State which parasite is depicted.
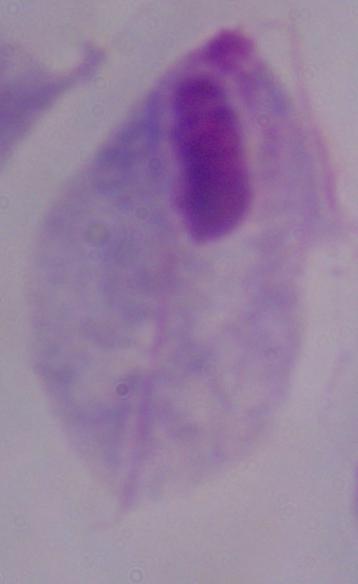

A trichomonad.

Captured at 1000x magnification. Micrograph.